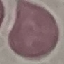
Summary:
  - Malaria status: uninfected
  - Image type: cell patch, automatically extracted from a larger field of view and resized to 64 × 64 pixels
  - Preparation: thin smear
  - Stain: Giemsa
  - Capture: smartphone camera at the microscope eyepiece